Report the malaria status of this cell.
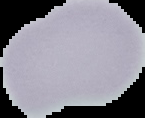
Uninfected.

{
  "image_size": "145×118 pixels",
  "preparation": "thin blood film",
  "image_type": "cell region segmented out of the field of view; surrounding area masked to black"
}